Assess for malaria.
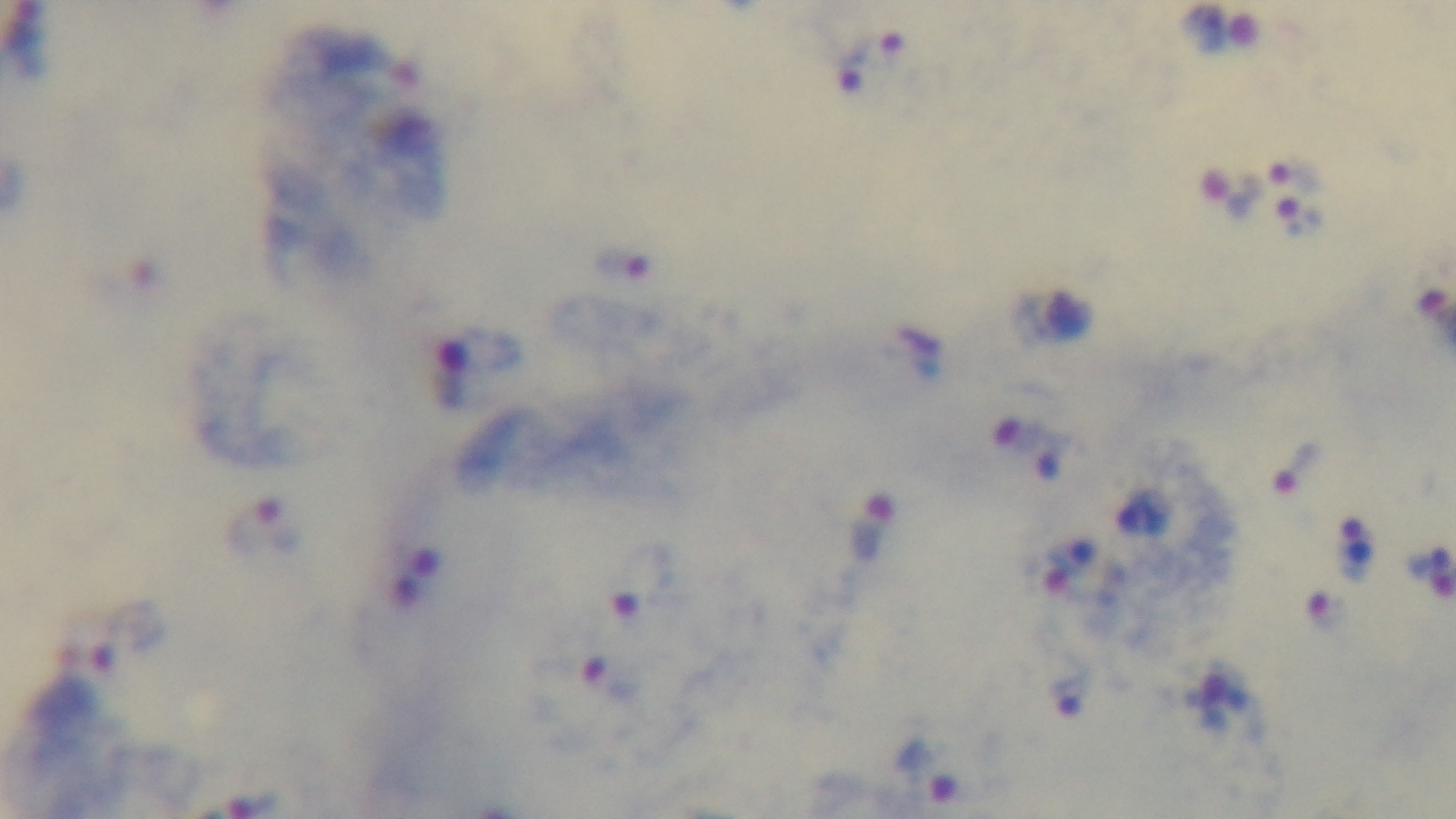
It is infected.

Giemsa-stained. Oil-immersion objective, 100x. Captured with a mounted 4K digital camera. Preparation: thick smear. Light microscopy. Single field of view.